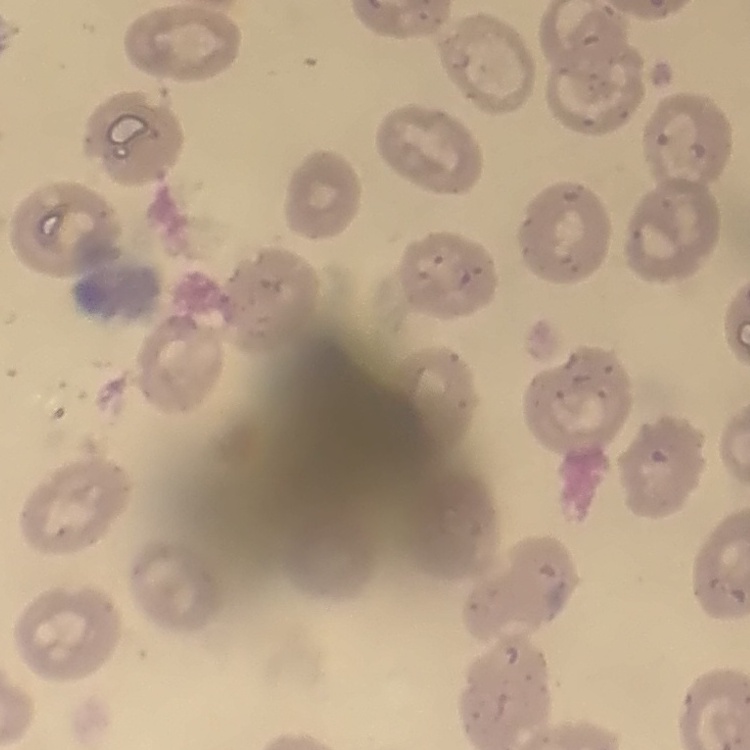
red blood cell morphology = no rouleaux formation
preparation = thin blood smear
image type = one tile cut from a larger photomicrograph
stain = Field's or Giemsa